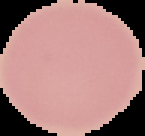
image_size: 145×136 pixels
image_type: segmented cell region on a black background
result: negative for Plasmodium parasites
preparation: thin blood smear